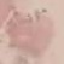

Summary:
  - Result: no malaria parasites detected
  - Stain: Giemsa
  - Preparation: thin smear
  - Capture: smartphone camera at the microscope eyepiece
  - Image type: cell patch, automatically extracted from a larger field of view and resized to 64 × 64 pixels